Identify the parasite.
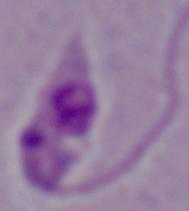

This is Leishmania.

Photomicrograph. 1000x magnification.